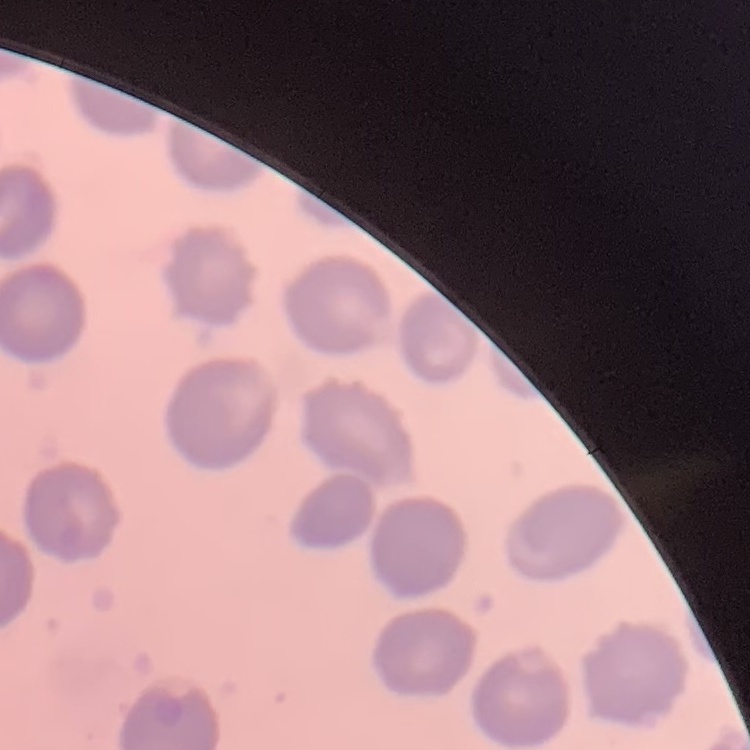
Summary:
  - Red blood cell morphology: no rouleaux formation
  - Image type: one tile cut from a larger photomicrograph
  - Preparation: thin peripheral smear
  - Stain: Field's or Giemsa